Point out each Plasmodium parasite.
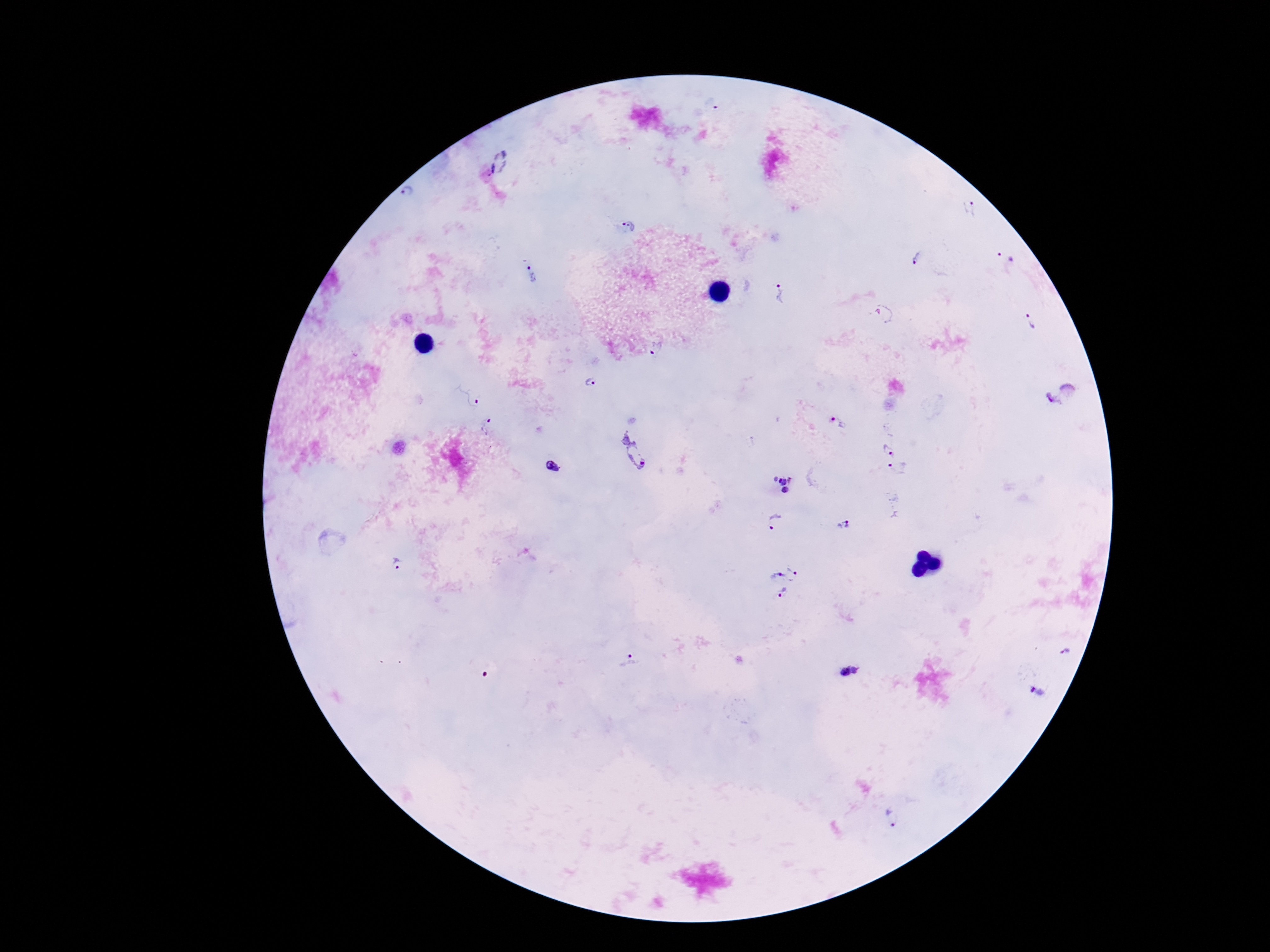

Approximate centers as (x, y) in pixels.
Plasmodium parasites: (500, 163), (409, 196), (970, 208), (627, 226), (917, 258), (1005, 261), (532, 273), (778, 293), (884, 313), (1028, 320), (655, 350), (589, 381), (1059, 393), (468, 394), (838, 423), (489, 428), (886, 446), (634, 449), (898, 466), (553, 467), (782, 483), (775, 521), (844, 524), (397, 565), (770, 574), (794, 575), (784, 599), (1065, 651), (629, 661), (851, 672), (1037, 691), (892, 819).

image size = 1270×952 pixels
stain = Giemsa
field of view = one from this slide
patient malaria status = positive
preparation = thick blood film
magnification = 100x
capture = smartphone camera through the microscope eyepiece